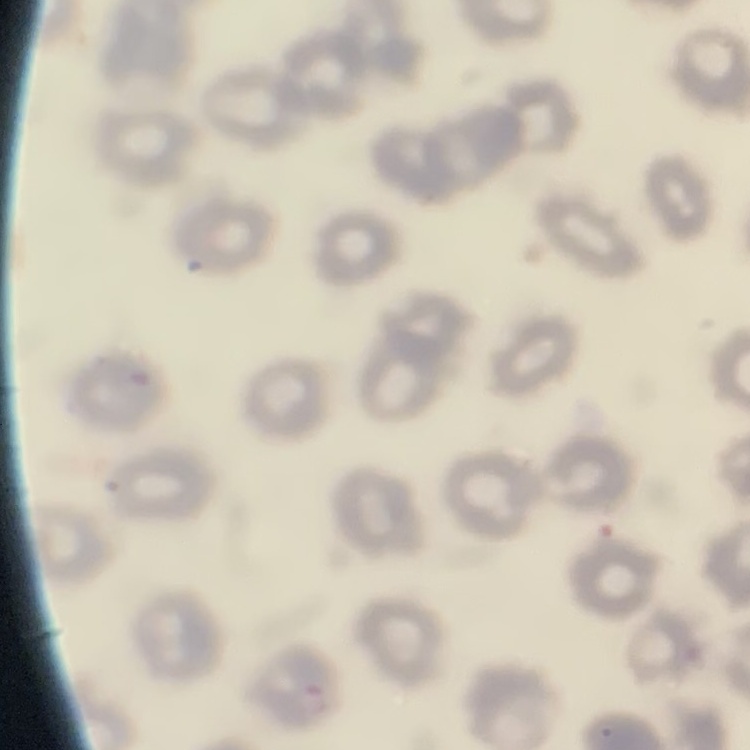
Summary:
  - Red blood cell morphology: no rouleaux formation
  - Stain: Field's or Giemsa
  - Preparation: thin blood film
  - Image type: square crop of a larger photomicrograph